Locate and identify every blood parasite.
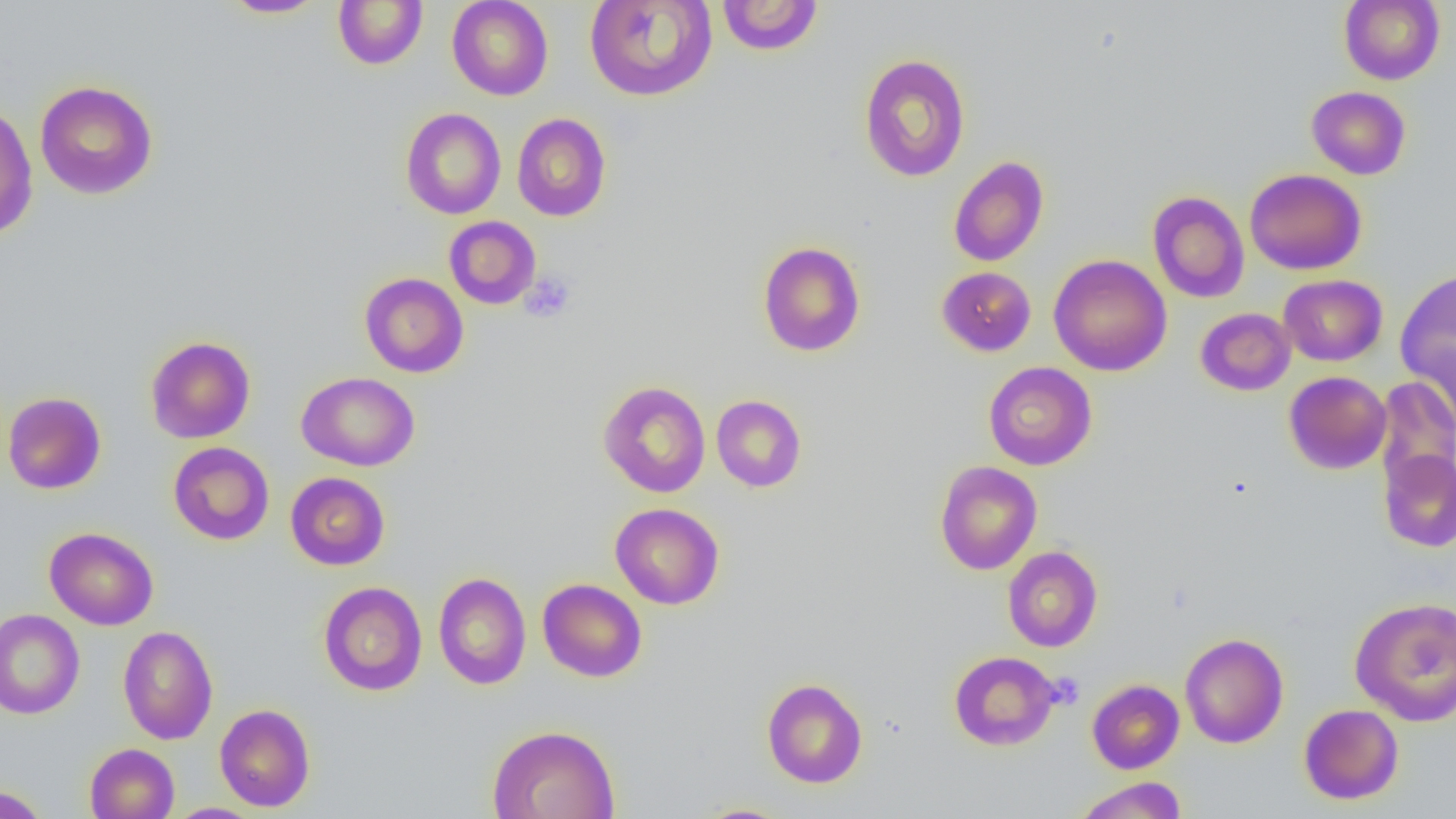
No blood parasites seen.

Approximate bounding boxes as named x1/y1/x2/y2 corners in pixels. Platelet locations: (x1=519, y1=272, x2=576, y2=323). Uninfected red blood cell locations: (x1=447, y1=0, x2=554, y2=100), (x1=584, y1=0, x2=718, y2=102), (x1=716, y1=0, x2=824, y2=56), (x1=1339, y1=0, x2=1445, y2=85), (x1=219, y1=1, x2=329, y2=18), (x1=332, y1=1, x2=428, y2=69), (x1=858, y1=54, x2=971, y2=182), (x1=34, y1=80, x2=158, y2=200), (x1=1306, y1=86, x2=1411, y2=179), (x1=0, y1=101, x2=38, y2=241), (x1=401, y1=107, x2=506, y2=219), (x1=512, y1=113, x2=611, y2=222), (x1=948, y1=156, x2=1049, y2=267), (x1=1245, y1=168, x2=1367, y2=275), (x1=1148, y1=191, x2=1249, y2=302), (x1=444, y1=216, x2=541, y2=309), (x1=757, y1=241, x2=866, y2=357), (x1=1048, y1=254, x2=1172, y2=376), (x1=936, y1=266, x2=1036, y2=356), (x1=1395, y1=268, x2=1456, y2=400), (x1=359, y1=272, x2=468, y2=378), (x1=1278, y1=274, x2=1387, y2=366), (x1=1195, y1=307, x2=1296, y2=396), (x1=1410, y1=333, x2=1456, y2=437), (x1=144, y1=335, x2=256, y2=443), (x1=983, y1=362, x2=1097, y2=470), (x1=296, y1=371, x2=420, y2=471), (x1=1284, y1=371, x2=1392, y2=474), (x1=1373, y1=376, x2=1456, y2=497), (x1=598, y1=380, x2=711, y2=498), (x1=1, y1=391, x2=106, y2=494), (x1=711, y1=394, x2=807, y2=492), (x1=168, y1=441, x2=274, y2=545), (x1=1379, y1=449, x2=1456, y2=552), (x1=934, y1=460, x2=1042, y2=575), (x1=285, y1=472, x2=390, y2=570), (x1=610, y1=503, x2=725, y2=609), (x1=44, y1=527, x2=159, y2=630), (x1=1002, y1=546, x2=1102, y2=652), (x1=433, y1=572, x2=531, y2=690), (x1=537, y1=579, x2=647, y2=682), (x1=318, y1=581, x2=428, y2=696), (x1=1349, y1=596, x2=1456, y2=727), (x1=0, y1=609, x2=85, y2=719), (x1=117, y1=625, x2=218, y2=745), (x1=1180, y1=632, x2=1289, y2=748), (x1=949, y1=651, x2=1060, y2=751), (x1=761, y1=677, x2=868, y2=788), (x1=1087, y1=679, x2=1185, y2=773), (x1=214, y1=703, x2=316, y2=811), (x1=1299, y1=703, x2=1404, y2=805), (x1=487, y1=724, x2=620, y2=819), (x1=84, y1=743, x2=179, y2=819), (x1=1073, y1=776, x2=1187, y2=819), (x1=0, y1=784, x2=50, y2=819), (x1=165, y1=803, x2=265, y2=819), (x1=691, y1=803, x2=798, y2=819). Slide-level diagnosis: no evidence of blood parasites. Thin blood smear. Optical microscopy. Image is 1456×819 pixels. One field of a larger specimen. Captured at 1000x magnification.